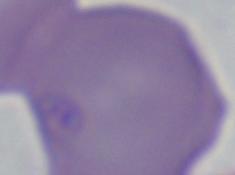
Summary:
  - Modality: photomicrograph
  - Identification: Babesia
  - Magnification: 1000x